Report the malaria status of this cell.
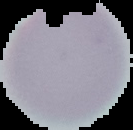
Uninfected.

Image is 133×130 pixels. From a thin blood smear. Segmented cell region on a black background.